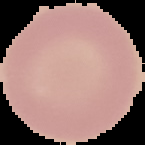
image type = segmented cell region on a black background
preparation = thin blood smear
image size = 145×145 pixels
result = no malaria parasites seen